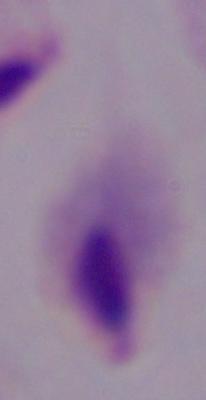 1000x magnification. Micrograph. A trichomonad is shown.